Identify the preparation type.
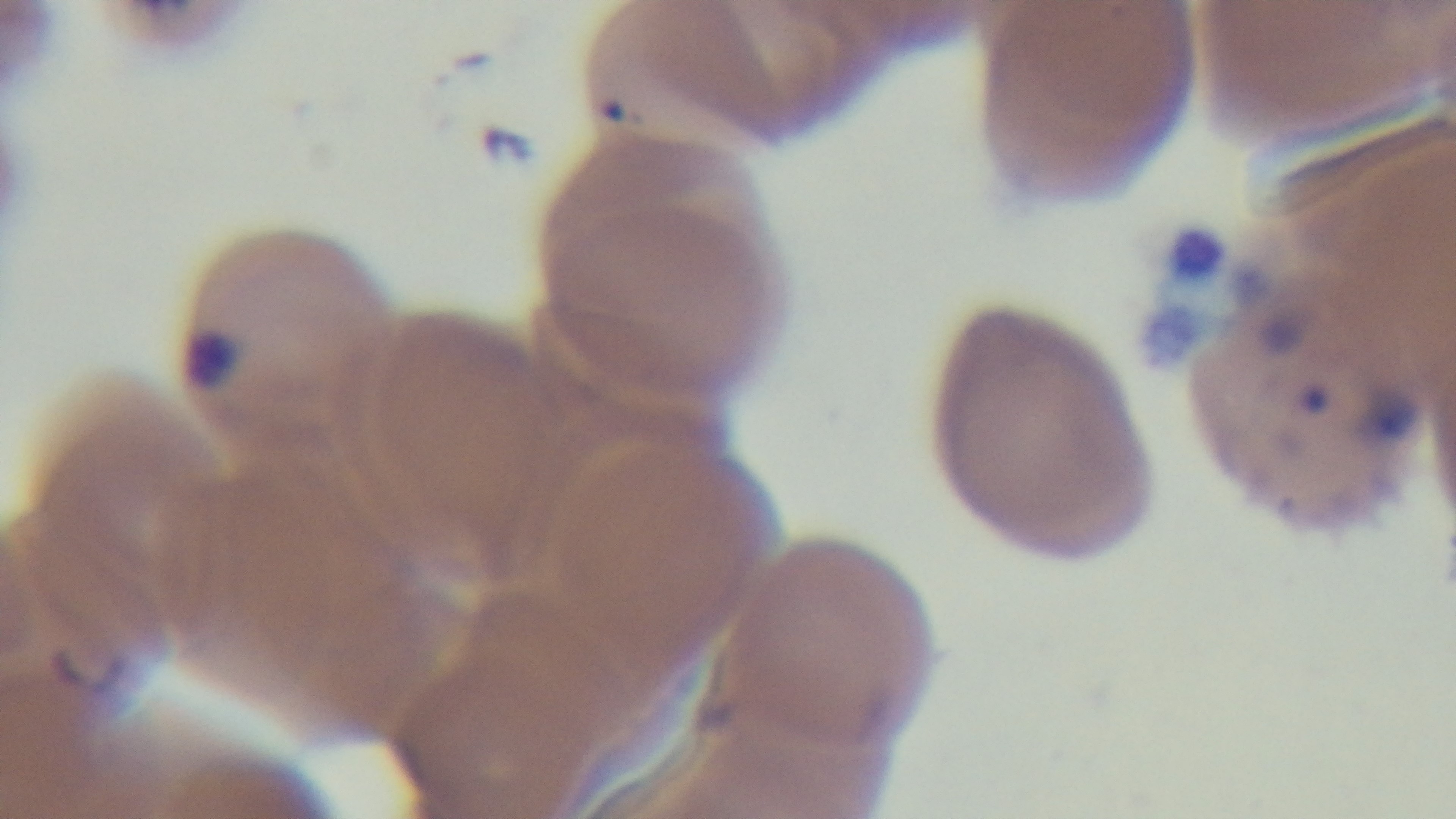
Thin.

objective = 100x oil immersion
capture = mounted 4K digital camera
malaria status = positive
field of view = single
modality = light microscopy
stain = Giemsa